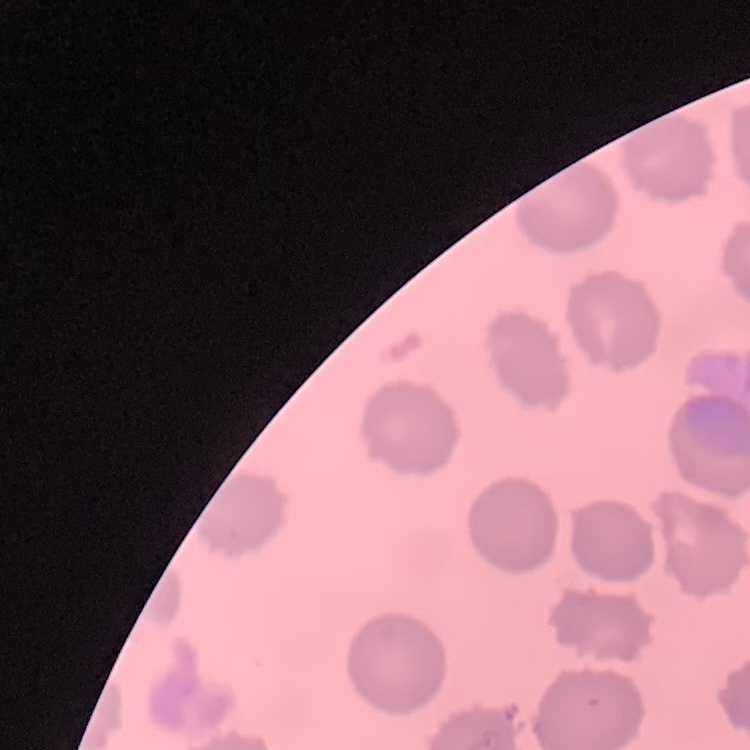

Summary:
  - Red blood cell morphology: no rouleaux formation
  - Image type: one tile cut from a larger photomicrograph
  - Preparation: thin blood smear
  - Stain: Field's or Giemsa